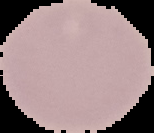
Summary:
  - Image size: 154×133 pixels
  - Image type: cell region segmented out of the field of view; surrounding area masked to black
  - Malaria status: uninfected
  - Preparation: thin blood film